Report the malaria status of this cell.
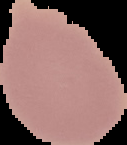
It is uninfected.

Cell region segmented out of the field of view; the surrounding area is masked to black. Image is 127×145 pixels. From a thin blood film.